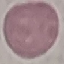 Malaria status: uninfected. Automatically extracted cell patch, resized to 64 × 64 pixels. Thin smear of blood. Giemsa-stained preparation. Acquired by smartphone through the microscope eyepiece.